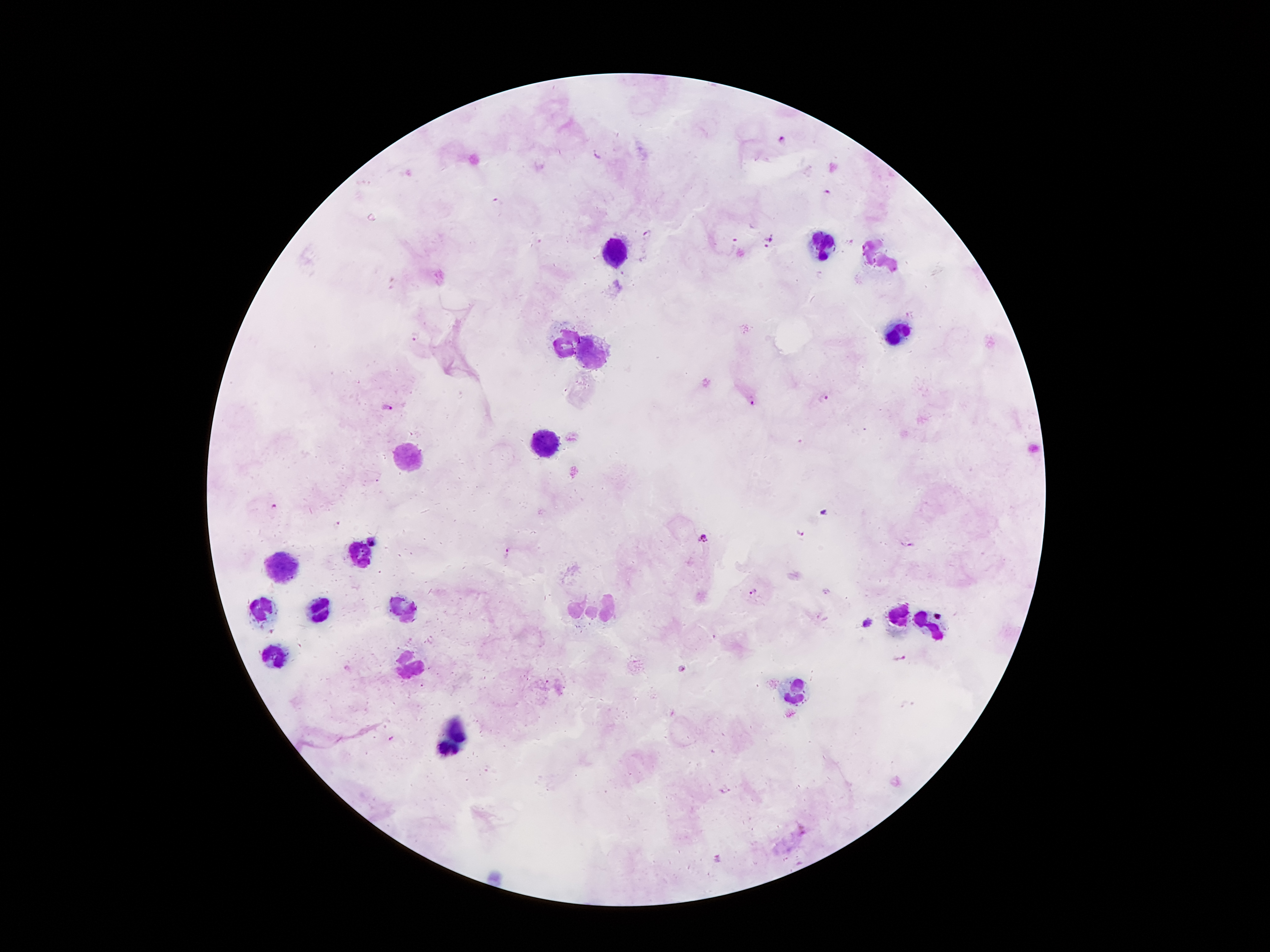 Approximate centers as {x, y} in pixels. Leukocyte locations: {822, 241}, {615, 254}, {897, 332}, {568, 341}, {595, 350}, {549, 447}, {408, 461}, {361, 557}, {282, 568}, {320, 606}, {263, 609}, {406, 609}, {583, 611}, {608, 611}, {897, 620}, {931, 629}, {275, 654}, {413, 663}, {797, 693}, {452, 738}. Malaria parasite locations: {783, 139}, {598, 155}, {828, 193}, {496, 200}, {649, 234}, {771, 238}, {734, 240}, {767, 247}, {415, 334}, {825, 397}, {752, 401}, {387, 407}, {273, 505}, {824, 514}, {338, 525}, {800, 533}, {703, 538}, {371, 540}, {912, 545}, {508, 553}, {754, 591}, {824, 591}, {866, 621}, {900, 657}, {682, 668}, {393, 739}, {727, 791}, {718, 859}. Image is 1270×952 pixels. 100x magnification. Giemsa-stained preparation. Thick peripheral-blood smear. Single field of view. Patient malaria status: positive for Plasmodium falciparum. Smartphone photograph taken through the microscope eyepiece.